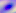

identification = Toxoplasma gondii
magnification = 400x
modality = micrograph